State which parasite is depicted.
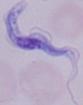

This is a trypanosome.

Summary:
  - Modality: photomicrograph
  - Magnification: 1000x